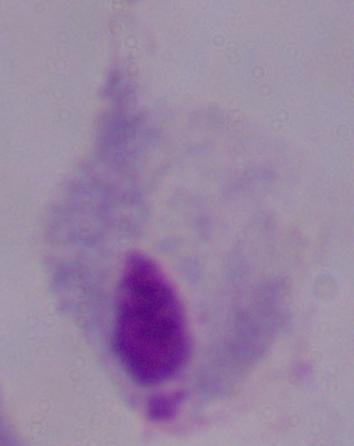

Summary:
  - Modality: photomicrograph
  - Magnification: 1000x
  - Identification: trichomonad